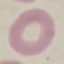
Malaria status: uninfected. Thin smear of blood. Giemsa stain. Automatically extracted cell patch, resized to 64 × 64 pixels. Photographed with a smartphone camera at the microscope eyepiece.